Locate every Plasmodium falciparum-infected red blood cell.
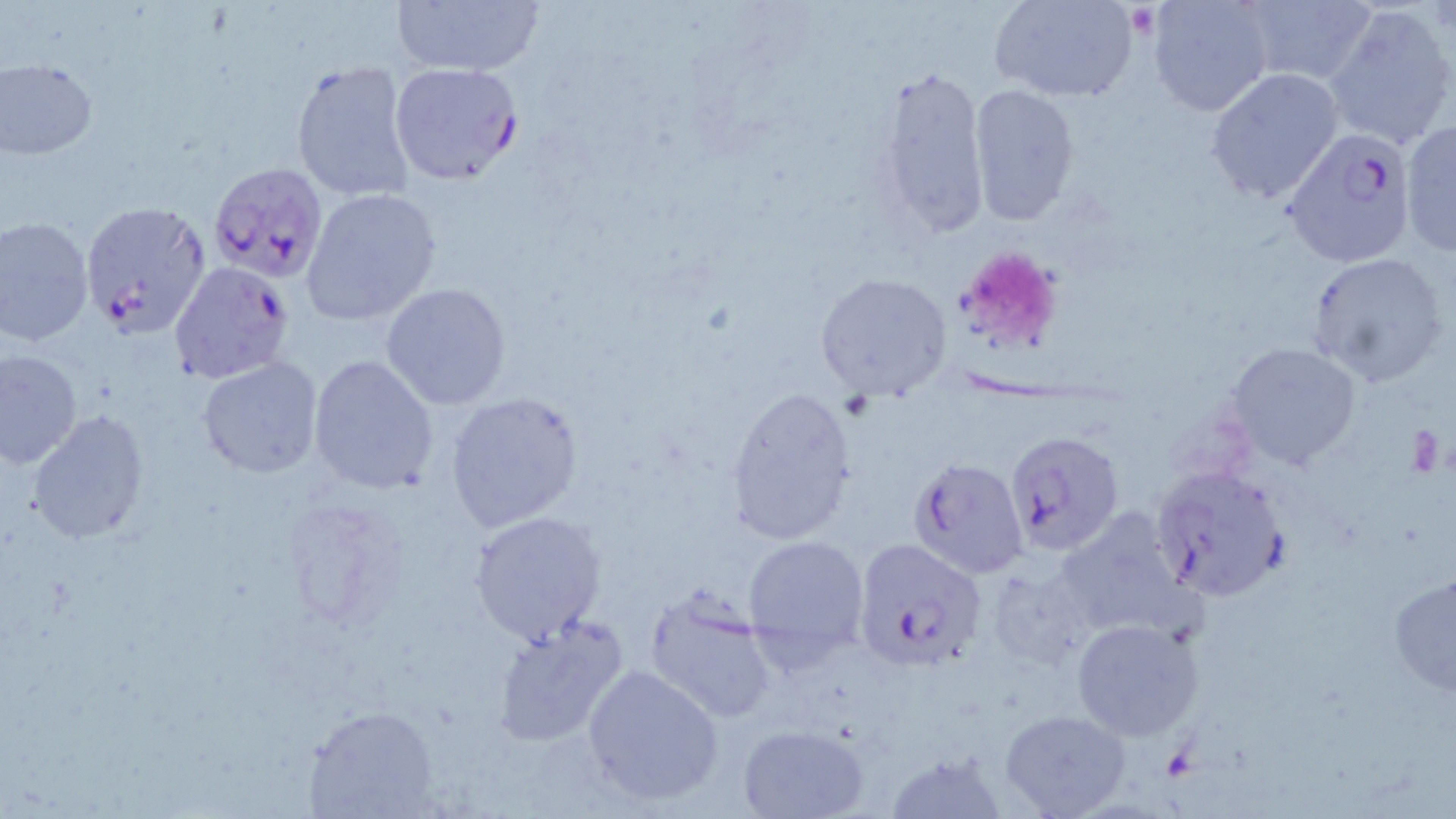
Approximate bounding boxes as [x1, y1, x2, y2] in pixels.
Plasmodium falciparum-infected red blood cells: [389, 62, 523, 185], [1282, 131, 1419, 270], [206, 161, 330, 283], [79, 200, 211, 337], [168, 261, 295, 385], [1003, 429, 1126, 557], [907, 457, 1029, 578], [1151, 465, 1291, 601], [852, 537, 987, 672].

Uninfected red blood cell locations: [390, 0, 546, 79], [994, 0, 1140, 102], [1148, 0, 1273, 115], [1234, 1, 1377, 90], [1323, 7, 1455, 151], [0, 59, 98, 158], [289, 59, 416, 203], [873, 64, 991, 240], [1206, 68, 1343, 205], [968, 84, 1080, 225], [1399, 121, 1456, 255], [301, 187, 443, 325], [0, 216, 95, 347], [1305, 252, 1450, 386], [815, 272, 953, 400], [380, 283, 513, 410], [1225, 342, 1360, 471], [0, 346, 83, 470], [309, 355, 440, 494], [198, 358, 323, 479], [725, 388, 857, 544], [444, 390, 585, 534], [27, 409, 150, 545], [1051, 506, 1195, 639], [468, 510, 605, 644], [742, 533, 871, 659], [1388, 572, 1456, 697], [644, 594, 777, 723], [491, 616, 630, 746], [1070, 616, 1206, 742], [583, 663, 724, 806], [306, 707, 439, 817], [1000, 709, 1131, 818], [735, 722, 874, 819]. Platelet locations: [955, 245, 1062, 351]. Slide-level diagnosis: Plasmodium falciparum. 1000x magnification. Optical microscopy. May-Grünwald-Giemsa stain. Image is 1456×819 pixels. One field of a larger specimen. Thin blood film.